Locate every Plasmodium malariae-infected red blood cell.
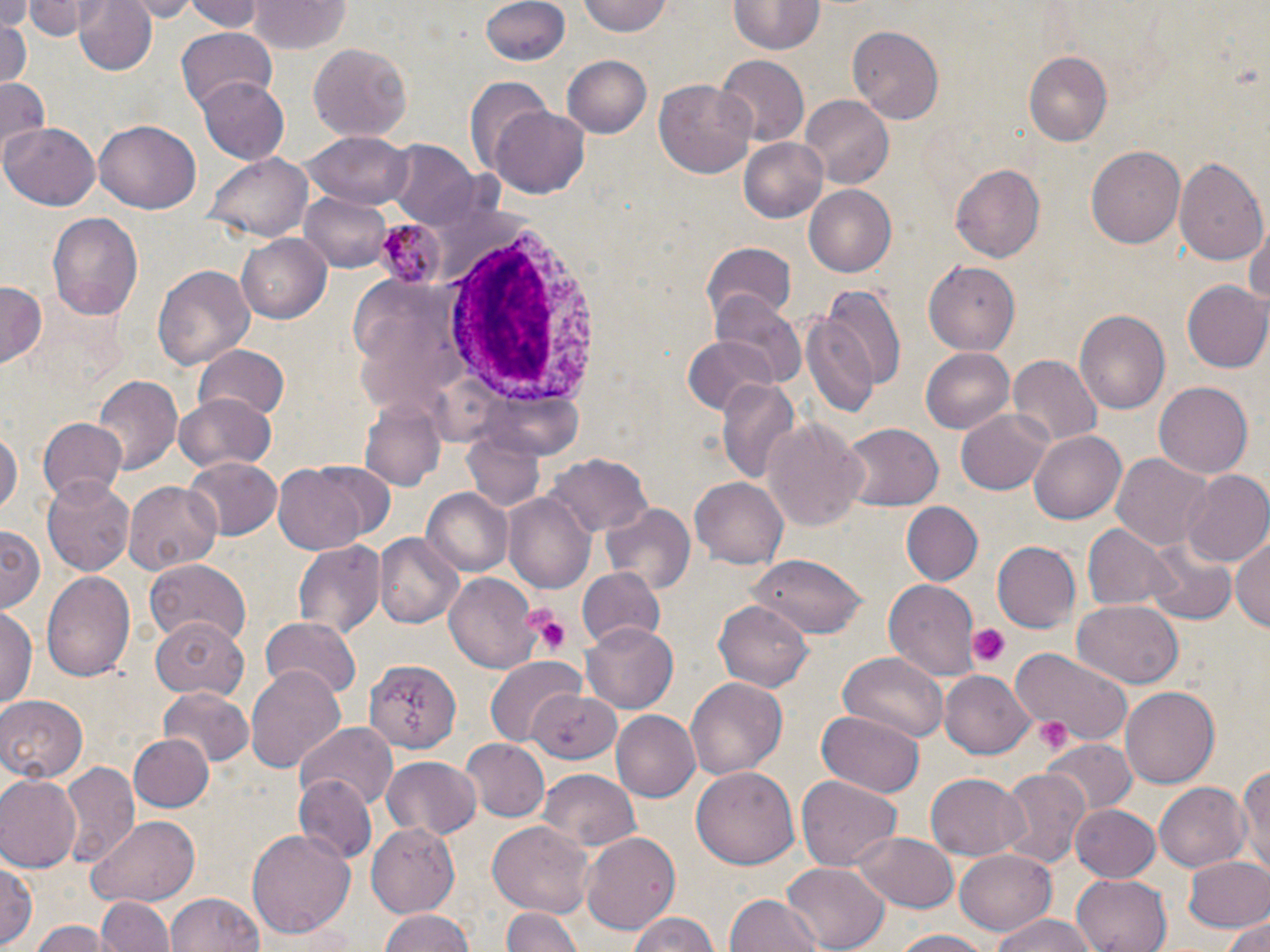
Approximate bounding boxes as named x1/y1/x2/y2 corners in pixels.
Plasmodium malariae-infected red blood cells: (x1=377, y1=220, x2=441, y2=286).

Uninfected red blood cell locations: (x1=24, y1=0, x2=91, y2=39), (x1=74, y1=0, x2=160, y2=78), (x1=123, y1=0, x2=206, y2=21), (x1=185, y1=0, x2=266, y2=33), (x1=252, y1=0, x2=351, y2=54), (x1=479, y1=0, x2=571, y2=66), (x1=579, y1=0, x2=672, y2=38), (x1=731, y1=1, x2=824, y2=55), (x1=0, y1=2, x2=30, y2=37), (x1=2, y1=15, x2=28, y2=91), (x1=849, y1=25, x2=944, y2=125), (x1=175, y1=30, x2=277, y2=114), (x1=309, y1=43, x2=412, y2=139), (x1=1024, y1=48, x2=1114, y2=148), (x1=714, y1=55, x2=806, y2=148), (x1=560, y1=57, x2=654, y2=139), (x1=198, y1=77, x2=290, y2=163), (x1=466, y1=77, x2=554, y2=172), (x1=0, y1=78, x2=51, y2=161), (x1=654, y1=80, x2=756, y2=180), (x1=802, y1=95, x2=894, y2=188), (x1=490, y1=105, x2=590, y2=198), (x1=96, y1=121, x2=200, y2=213), (x1=3, y1=123, x2=100, y2=210), (x1=304, y1=132, x2=413, y2=210), (x1=739, y1=136, x2=829, y2=223), (x1=388, y1=143, x2=483, y2=231), (x1=1087, y1=143, x2=1186, y2=250), (x1=206, y1=154, x2=311, y2=242), (x1=1174, y1=156, x2=1268, y2=265), (x1=951, y1=163, x2=1046, y2=263), (x1=803, y1=185, x2=897, y2=278), (x1=299, y1=191, x2=394, y2=270), (x1=47, y1=208, x2=145, y2=322), (x1=1247, y1=219, x2=1270, y2=317), (x1=237, y1=231, x2=331, y2=324), (x1=702, y1=242, x2=797, y2=322), (x1=925, y1=258, x2=1024, y2=355), (x1=153, y1=264, x2=255, y2=370), (x1=1182, y1=281, x2=1270, y2=374), (x1=0, y1=283, x2=47, y2=367), (x1=819, y1=284, x2=905, y2=398), (x1=709, y1=293, x2=805, y2=387), (x1=1073, y1=307, x2=1169, y2=417), (x1=800, y1=312, x2=880, y2=418), (x1=681, y1=335, x2=781, y2=416), (x1=194, y1=345, x2=289, y2=424), (x1=921, y1=347, x2=1017, y2=434), (x1=1008, y1=354, x2=1100, y2=446), (x1=91, y1=376, x2=182, y2=478), (x1=716, y1=378, x2=799, y2=481), (x1=1152, y1=381, x2=1253, y2=478), (x1=174, y1=395, x2=279, y2=474), (x1=360, y1=398, x2=447, y2=491), (x1=956, y1=409, x2=1054, y2=495), (x1=762, y1=415, x2=871, y2=535), (x1=0, y1=419, x2=21, y2=528), (x1=37, y1=419, x2=127, y2=502), (x1=838, y1=424, x2=944, y2=511), (x1=1027, y1=428, x2=1127, y2=523), (x1=464, y1=429, x2=543, y2=508), (x1=548, y1=453, x2=652, y2=539), (x1=1113, y1=454, x2=1213, y2=552), (x1=185, y1=458, x2=281, y2=539), (x1=270, y1=463, x2=377, y2=556), (x1=1181, y1=470, x2=1270, y2=568), (x1=42, y1=477, x2=134, y2=576), (x1=690, y1=478, x2=787, y2=568), (x1=123, y1=482, x2=223, y2=573), (x1=422, y1=488, x2=512, y2=576), (x1=503, y1=491, x2=594, y2=594), (x1=902, y1=501, x2=983, y2=586), (x1=602, y1=503, x2=695, y2=595), (x1=1084, y1=524, x2=1177, y2=610), (x1=0, y1=527, x2=43, y2=614), (x1=1232, y1=531, x2=1270, y2=635), (x1=375, y1=534, x2=463, y2=631), (x1=1142, y1=538, x2=1236, y2=625), (x1=293, y1=540, x2=385, y2=640), (x1=992, y1=541, x2=1082, y2=633), (x1=748, y1=554, x2=872, y2=638), (x1=145, y1=558, x2=251, y2=647), (x1=576, y1=568, x2=665, y2=652), (x1=41, y1=569, x2=136, y2=683), (x1=444, y1=571, x2=544, y2=672), (x1=884, y1=580, x2=980, y2=683), (x1=714, y1=599, x2=815, y2=691), (x1=1075, y1=600, x2=1184, y2=686), (x1=0, y1=604, x2=36, y2=711), (x1=261, y1=618, x2=361, y2=701), (x1=150, y1=619, x2=246, y2=700), (x1=581, y1=622, x2=678, y2=711), (x1=1009, y1=647, x2=1134, y2=745), (x1=838, y1=651, x2=949, y2=746), (x1=484, y1=657, x2=585, y2=747), (x1=366, y1=660, x2=462, y2=752), (x1=246, y1=664, x2=346, y2=773), (x1=938, y1=672, x2=1034, y2=757), (x1=685, y1=676, x2=788, y2=778), (x1=159, y1=686, x2=253, y2=765), (x1=1120, y1=687, x2=1220, y2=789), (x1=527, y1=688, x2=621, y2=762), (x1=0, y1=694, x2=88, y2=783), (x1=819, y1=708, x2=926, y2=797), (x1=611, y1=711, x2=700, y2=802), (x1=296, y1=723, x2=399, y2=810), (x1=127, y1=734, x2=213, y2=814), (x1=1042, y1=738, x2=1136, y2=818), (x1=461, y1=739, x2=547, y2=822), (x1=381, y1=757, x2=481, y2=842), (x1=1236, y1=759, x2=1269, y2=874), (x1=60, y1=761, x2=140, y2=865), (x1=692, y1=765, x2=800, y2=870), (x1=994, y1=767, x2=1091, y2=874), (x1=538, y1=770, x2=640, y2=856), (x1=926, y1=771, x2=1027, y2=859), (x1=0, y1=774, x2=81, y2=872), (x1=297, y1=776, x2=376, y2=866), (x1=795, y1=776, x2=903, y2=870), (x1=1153, y1=781, x2=1248, y2=871), (x1=1072, y1=805, x2=1161, y2=883), (x1=87, y1=813, x2=202, y2=904), (x1=487, y1=822, x2=595, y2=917), (x1=366, y1=824, x2=460, y2=918), (x1=248, y1=828, x2=357, y2=937), (x1=580, y1=831, x2=680, y2=937), (x1=851, y1=833, x2=959, y2=911), (x1=957, y1=848, x2=1057, y2=934), (x1=1183, y1=855, x2=1270, y2=934), (x1=0, y1=856, x2=39, y2=950), (x1=782, y1=860, x2=888, y2=951), (x1=1072, y1=875, x2=1170, y2=952), (x1=165, y1=892, x2=265, y2=952), (x1=724, y1=894, x2=824, y2=952), (x1=94, y1=895, x2=176, y2=952), (x1=499, y1=906, x2=585, y2=952), (x1=376, y1=908, x2=475, y2=952), (x1=623, y1=912, x2=726, y2=952), (x1=988, y1=913, x2=1101, y2=952), (x1=1222, y1=915, x2=1270, y2=952), (x1=26, y1=919, x2=115, y2=951), (x1=890, y1=929, x2=997, y2=952). White blood cell locations: (x1=430, y1=219, x2=611, y2=424). Platelet locations: (x1=522, y1=606, x2=571, y2=657), (x1=968, y1=624, x2=1010, y2=667), (x1=1035, y1=715, x2=1074, y2=755). Slide-level diagnosis: Plasmodium malariae. One field of a larger specimen. Light microscopy. Image is 1270×952 pixels. 1000x magnification. May-Grünwald-Giemsa-stained preparation. Thin blood smear.